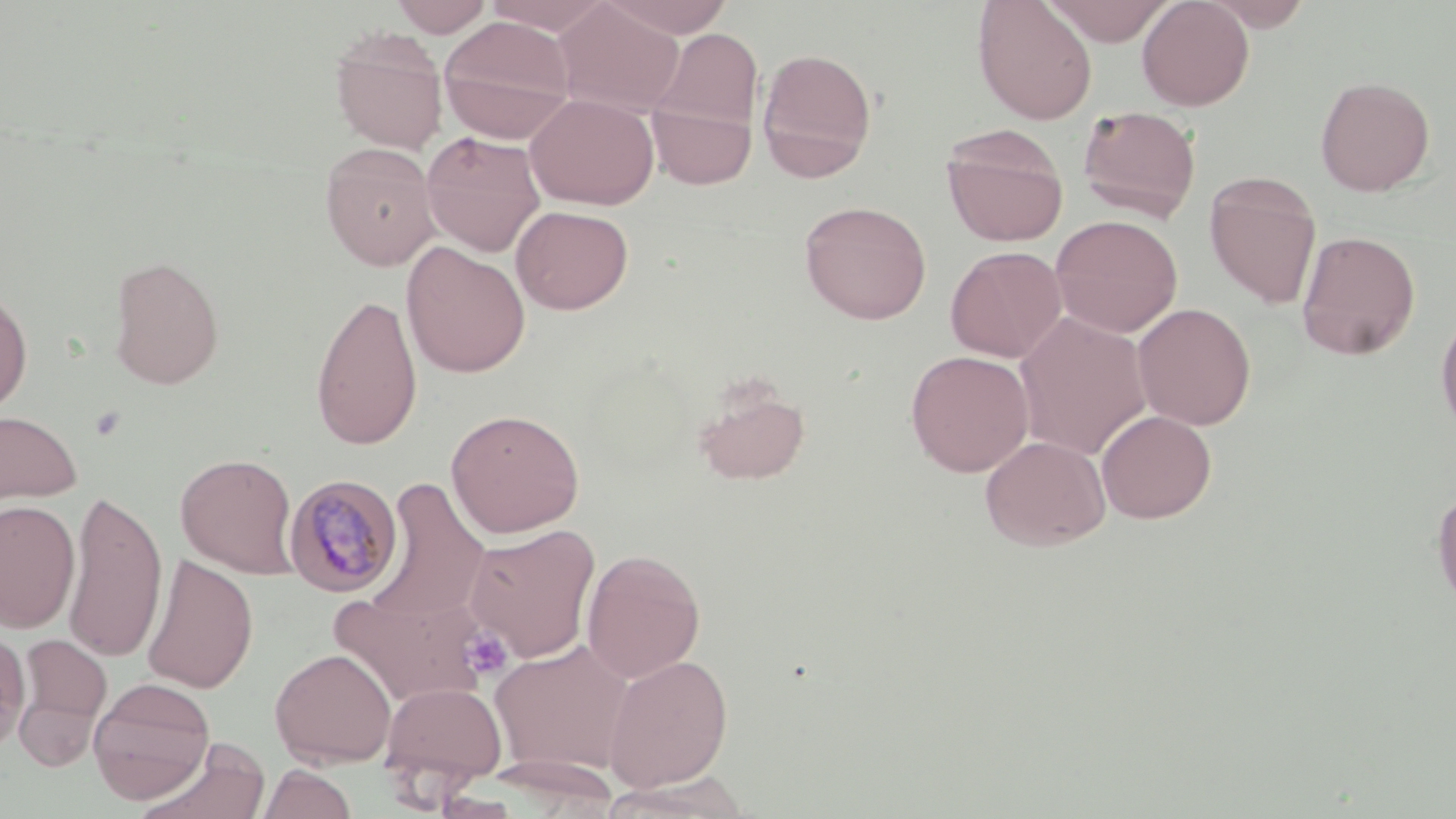 Approximate bounding boxes as (x1, y1, x2, y2) in pixels. Uninfected red blood cell locations: (391, 0, 493, 37), (481, 0, 617, 36), (603, 0, 735, 38), (972, 0, 1098, 125), (1043, 0, 1176, 45), (1137, 0, 1255, 111), (1200, 0, 1315, 31), (554, 1, 684, 118), (438, 16, 575, 142), (330, 29, 448, 154), (651, 29, 764, 135), (756, 46, 878, 181), (1315, 75, 1435, 196), (525, 93, 659, 210), (647, 99, 757, 189), (1077, 105, 1202, 223), (942, 126, 1069, 246), (421, 131, 546, 256), (320, 142, 441, 271), (1204, 173, 1322, 310), (799, 200, 932, 325), (510, 205, 634, 314), (1051, 215, 1183, 338), (1296, 230, 1420, 361), (401, 241, 531, 378), (945, 245, 1067, 363), (107, 255, 225, 389), (0, 285, 34, 419), (310, 292, 423, 451), (1133, 302, 1256, 430), (1435, 309, 1456, 438), (1015, 311, 1152, 461), (905, 350, 1035, 476), (692, 381, 811, 487), (0, 408, 82, 507), (446, 408, 585, 538), (1096, 410, 1217, 524), (980, 435, 1111, 551), (176, 453, 299, 578), (367, 478, 491, 627), (1431, 484, 1456, 614), (65, 491, 167, 663), (0, 500, 80, 634), (463, 524, 601, 663), (581, 548, 706, 683), (141, 555, 258, 694), (329, 587, 490, 707), (0, 628, 31, 756), (13, 633, 111, 762), (490, 638, 636, 777), (270, 648, 396, 767), (603, 654, 734, 792), (87, 677, 216, 804), (379, 681, 508, 791), (136, 739, 271, 819), (258, 764, 357, 819). Plasmodium malariae-infected red blood cell locations: (283, 474, 403, 597). Platelet locations: (460, 626, 514, 681). Slide-level diagnosis: Plasmodium malariae. Light microscopy. 1000x magnification. May-Grünwald-Giemsa-stained preparation. Single field of view. Thin blood film. Image is 1456×819 pixels.